State which cell type is depicted.
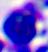
A leukocyte.

Photomicrograph. Captured at 400x magnification.